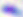
magnification = 400x
identification = Toxoplasma gondii
modality = micrograph